Look for Plasmodium parasites.
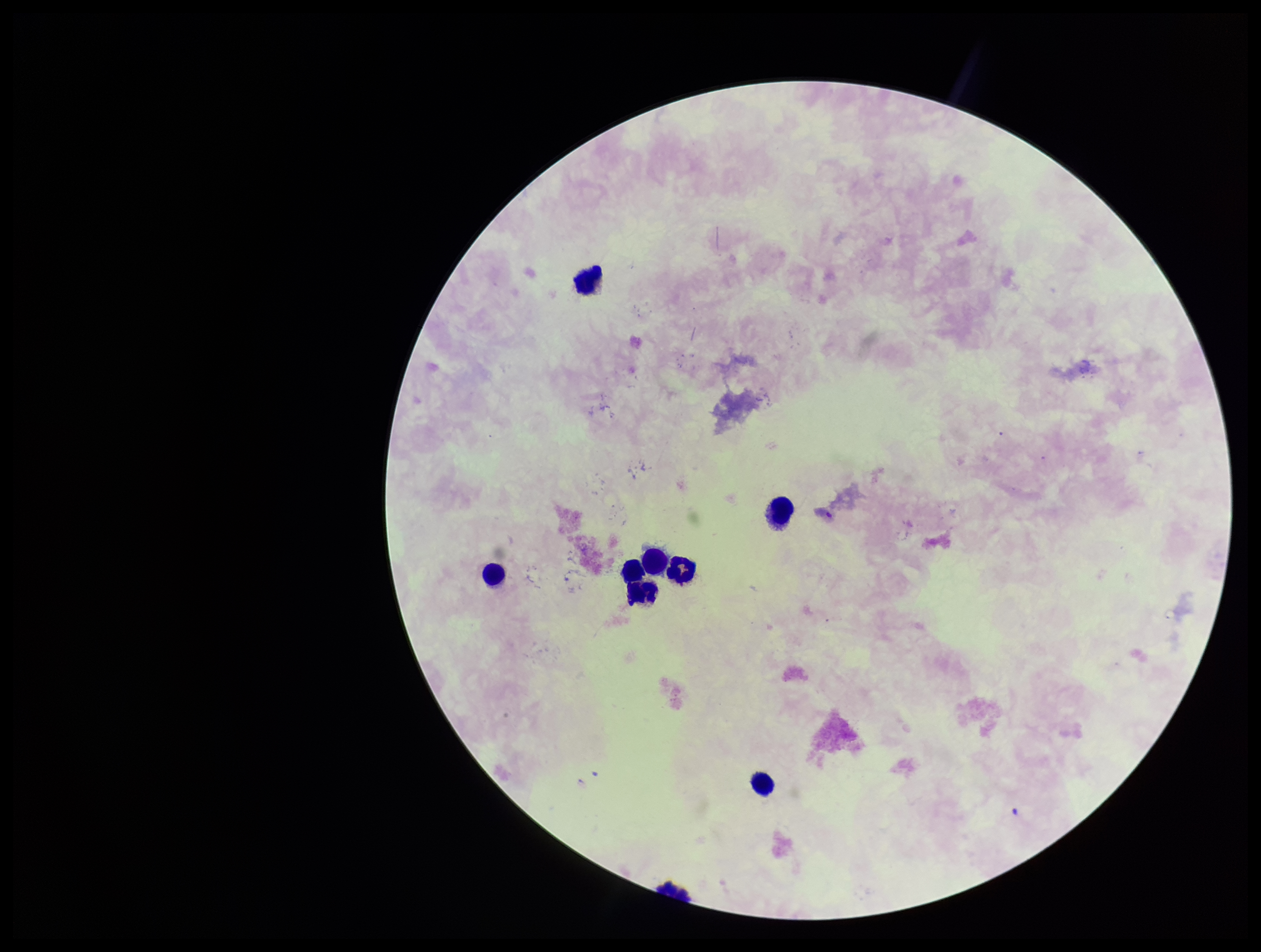

None seen.

capture: smartphone photograph through the microscope eyepiece
preparation: thick smear
stain: Giemsa
field_of_view: single
patient_malaria_status: negative
leukocyte_count: 7
parasite_count: 0
image_size: 1261×952 pixels